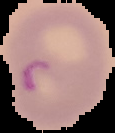

Summary:
  - Result: Plasmodium parasites detected
  - Preparation: thin blood film
  - Image size: 115×133 pixels
  - Image type: cell region segmented out of the field of view; surrounding area masked to black